Assess this cell for malaria.
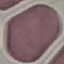

Uninfected.

{
  "stain": "Giemsa",
  "preparation": "thin smear",
  "capture": "smartphone through the microscope eyepiece",
  "image_type": "cell patch, automatically extracted from a larger field of view and resized to 64 × 64 pixels"
}